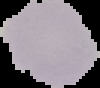
Image is 100×88 pixels. Malaria status: uninfected. Cell region segmented out of the field of view; the surrounding area is masked to black. From a thin blood smear.